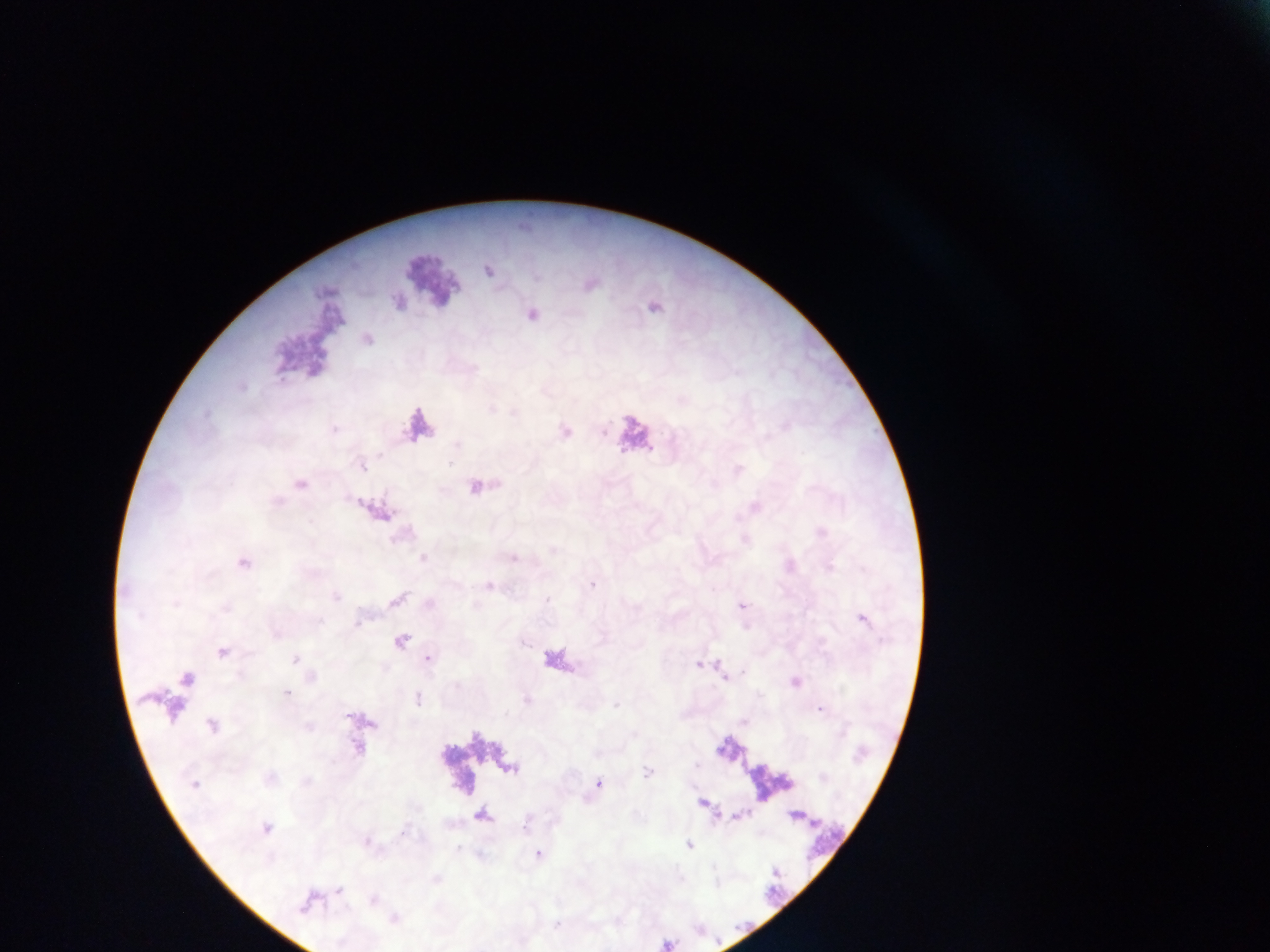 Approximate centers as (x, y) in pixels. Leukocyte locations: (430, 281), (634, 433), (556, 661). Malaria parasite locations: (488, 270), (653, 307), (531, 314), (366, 338), (565, 432), (738, 471), (299, 484), (475, 486), (754, 506), (376, 511), (423, 558), (242, 563), (592, 583), (488, 584), (335, 597), (396, 599), (742, 605), (862, 619), (400, 640), (222, 651), (427, 658), (295, 659), (700, 664), (725, 676), (187, 678), (795, 681), (286, 693), (418, 698), (820, 709), (213, 725), (647, 771), (194, 783), (598, 783), (702, 803), (265, 827), (688, 844), (537, 853), (372, 899), (307, 901), (394, 919). Single field of view. Image is 1270×952 pixels. Thick blood film. Mobile-phone photograph taken through the microscope. Sample from Ghana.